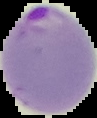 Segmented cell region on a black background. Result: malaria parasites identified. From a thin blood film. Image is 97×118 pixels.